Classify this cell by malaria status.
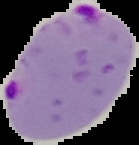

It is parasitized.

From a thin blood smear. The area outside the segmented cell region is set to black. Image is 139×145 pixels.